Identify the cell.
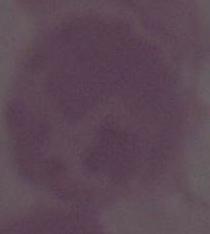
This is an erythrocyte.

Summary:
  - Magnification: 1000x
  - Modality: photomicrograph